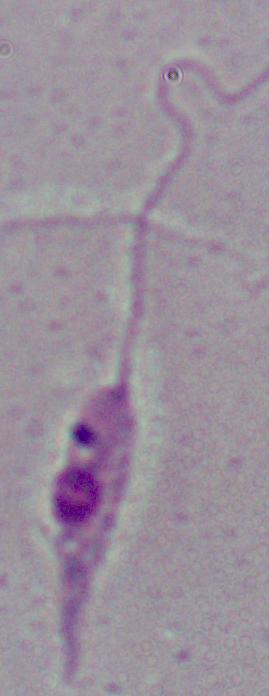
Summary:
  - Modality: micrograph
  - Identification: Leishmania
  - Magnification: 1000x